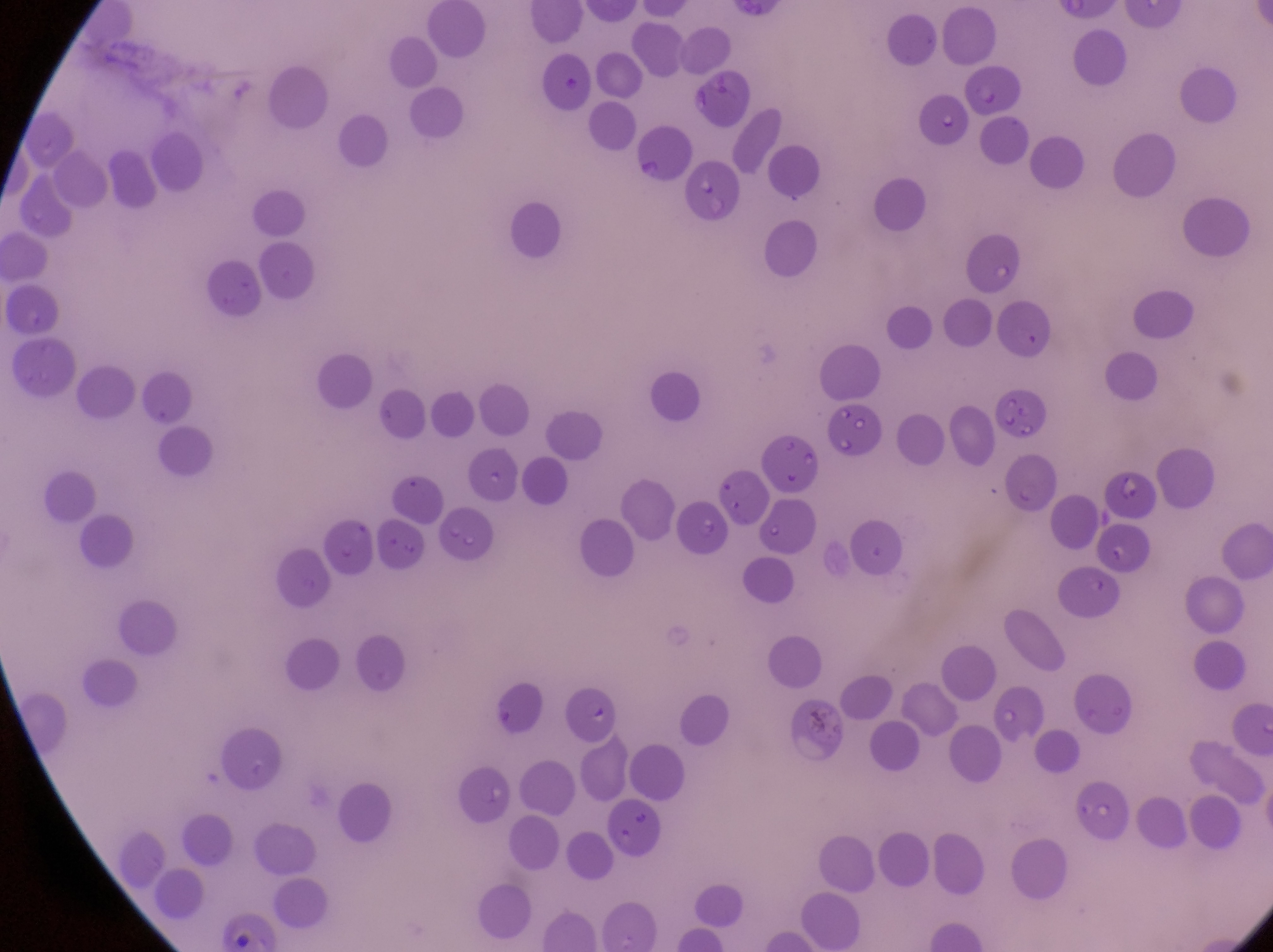

Approximate bounding boxes as (left, top, right, bottom) in pixels.
Summary:
  - Parasitised red blood cell locations: (966, 63, 1023, 121), (921, 100, 971, 152), (636, 127, 693, 187), (826, 407, 886, 455), (564, 687, 616, 747)
  - Artifact (platelet-like body, stain precipitate, or debris) locations: (801, 700, 861, 757)
  - Field of view: single
  - Magnification: 1000x
  - Preparation: thin blood film
  - Country: Uganda
  - Capture: smartphone photograph through the eyepiece of an Olympus CX-23 microscope
  - Image size: 1273×952 pixels